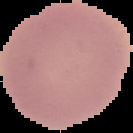
Segmented cell region on a black background. Image is 133×133 pixels. Result: no malaria parasites seen. From a thin blood smear.